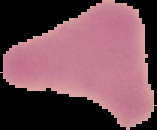

Summary:
  - Result: negative for Plasmodium parasites
  - Image type: segmented cell region with the area outside set to black
  - Preparation: thin blood smear
  - Image size: 157×130 pixels